Name the parasite shown.
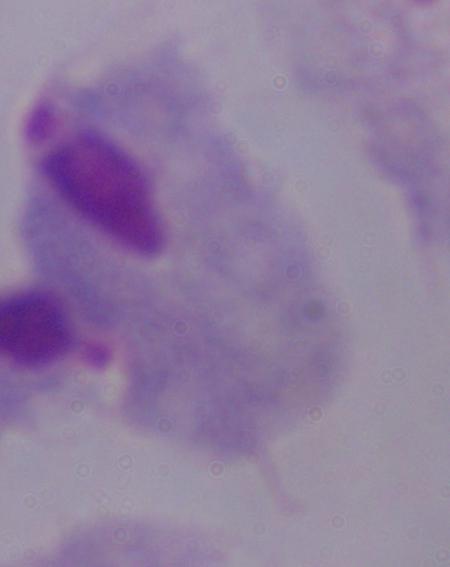
A trichomonad.

Photomicrograph. Captured at 1000x magnification.